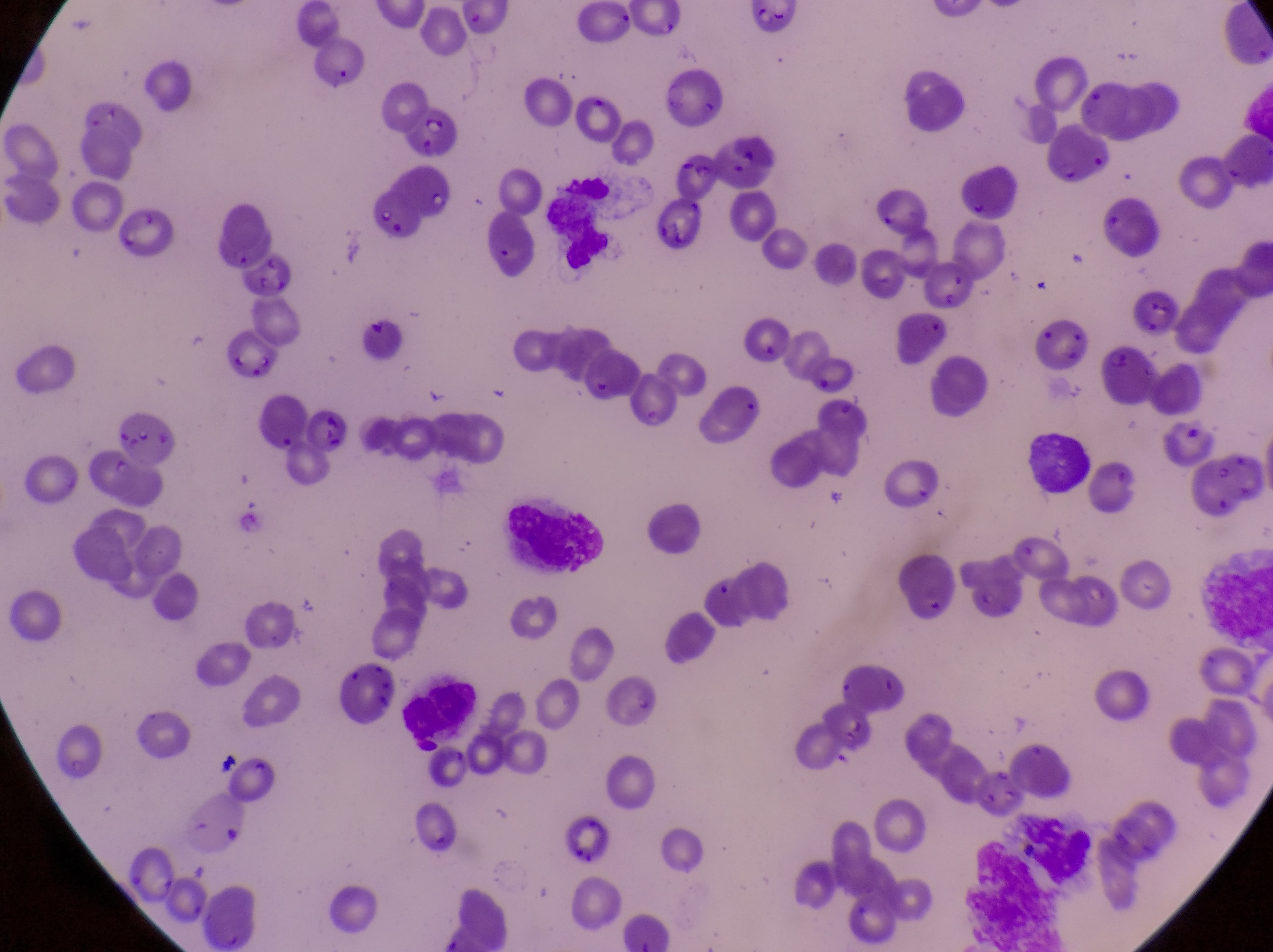
image size = 1273×952 pixels
capture = smartphone photograph through the eyepiece of an Olympus CX-23 microscope
country = Uganda
preparation = thin blood film
magnification = 1000x
leukocyte locations = approximate bounding boxes as {left, top, right, bottom} in pixels: {1029, 422, 1092, 492}, {482, 482, 609, 584}, {397, 683, 481, 744}, {1011, 810, 1094, 886}
field of view = single
parasitised red blood cell locations = approximate bounding boxes as {left, top, right, bottom} in pixels: {399, 104, 449, 161}, {669, 145, 721, 198}, {112, 210, 178, 265}, {1123, 294, 1181, 339}, {221, 336, 284, 386}, {1103, 344, 1160, 407}, {893, 559, 965, 626}, {329, 668, 395, 734}